Locate and identify every blood parasite.
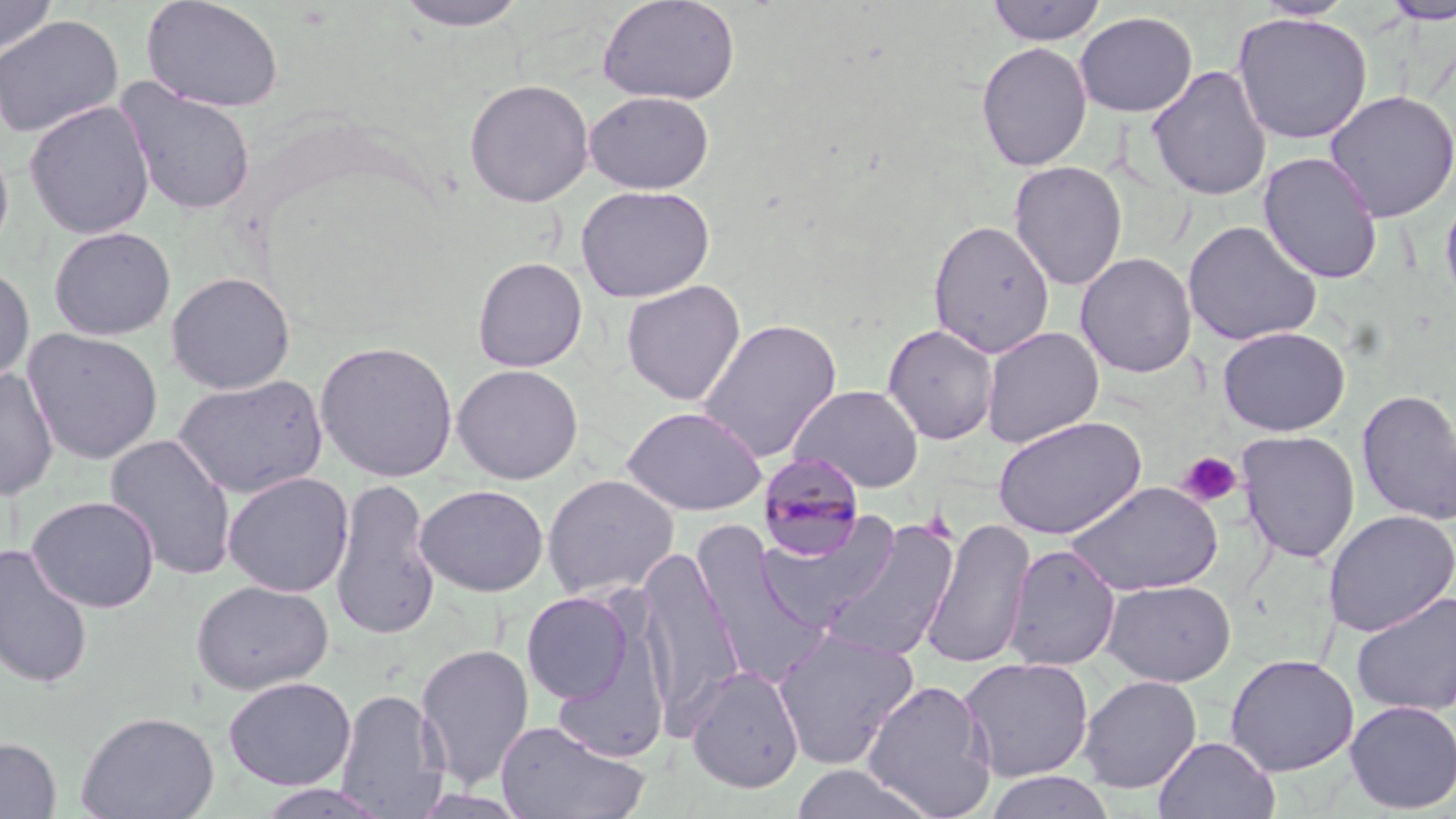
Approximate bounding boxes as named x1/y1/x2/y2 corners in pixels.
Plasmodium malariae-infected red blood cells: (x1=754, y1=453, x2=868, y2=559).
No Plasmodium falciparum, Plasmodium ovale, Plasmodium vivax, Babesia divergens, or Trypanosoma brucei observed.

Summary:
  - Uninfected red blood cell locations: (x1=0, y1=0, x2=59, y2=58), (x1=141, y1=0, x2=285, y2=113), (x1=390, y1=0, x2=533, y2=32), (x1=596, y1=0, x2=741, y2=105), (x1=985, y1=0, x2=1107, y2=46), (x1=1380, y1=0, x2=1456, y2=25), (x1=1252, y1=1, x2=1357, y2=22), (x1=1073, y1=11, x2=1198, y2=117), (x1=1231, y1=11, x2=1373, y2=145), (x1=0, y1=15, x2=124, y2=139), (x1=976, y1=41, x2=1092, y2=172), (x1=1146, y1=65, x2=1273, y2=201), (x1=463, y1=78, x2=595, y2=208), (x1=117, y1=81, x2=257, y2=217), (x1=1324, y1=89, x2=1456, y2=224), (x1=584, y1=91, x2=715, y2=194), (x1=23, y1=100, x2=156, y2=240), (x1=0, y1=131, x2=15, y2=264), (x1=1258, y1=152, x2=1383, y2=285), (x1=1008, y1=160, x2=1128, y2=291), (x1=575, y1=184, x2=716, y2=303), (x1=1440, y1=185, x2=1456, y2=314), (x1=928, y1=218, x2=1055, y2=358), (x1=1183, y1=220, x2=1323, y2=347), (x1=48, y1=226, x2=176, y2=341), (x1=1075, y1=252, x2=1197, y2=377), (x1=471, y1=256, x2=588, y2=372), (x1=0, y1=264, x2=35, y2=389), (x1=166, y1=271, x2=296, y2=395), (x1=621, y1=279, x2=746, y2=405), (x1=696, y1=317, x2=842, y2=464), (x1=882, y1=323, x2=999, y2=445), (x1=981, y1=326, x2=1104, y2=448), (x1=1218, y1=326, x2=1350, y2=436), (x1=22, y1=327, x2=163, y2=465), (x1=315, y1=339, x2=459, y2=483), (x1=452, y1=363, x2=583, y2=484), (x1=0, y1=368, x2=59, y2=501), (x1=172, y1=374, x2=328, y2=499), (x1=790, y1=384, x2=923, y2=493), (x1=1356, y1=389, x2=1456, y2=526), (x1=621, y1=405, x2=767, y2=515), (x1=992, y1=415, x2=1147, y2=540), (x1=1236, y1=430, x2=1360, y2=563), (x1=103, y1=432, x2=238, y2=580), (x1=221, y1=471, x2=354, y2=597), (x1=542, y1=473, x2=680, y2=600), (x1=330, y1=477, x2=440, y2=643), (x1=1066, y1=480, x2=1224, y2=596), (x1=415, y1=483, x2=549, y2=597), (x1=27, y1=496, x2=159, y2=612), (x1=1323, y1=510, x2=1456, y2=637), (x1=757, y1=513, x2=899, y2=630), (x1=819, y1=517, x2=960, y2=663), (x1=920, y1=517, x2=1035, y2=669), (x1=693, y1=528, x2=832, y2=688), (x1=1004, y1=542, x2=1120, y2=671), (x1=0, y1=543, x2=93, y2=689), (x1=640, y1=546, x2=745, y2=719), (x1=1100, y1=579, x2=1237, y2=687), (x1=191, y1=580, x2=334, y2=694), (x1=1349, y1=589, x2=1456, y2=717), (x1=521, y1=591, x2=635, y2=705), (x1=771, y1=627, x2=920, y2=770), (x1=415, y1=641, x2=535, y2=791), (x1=1224, y1=653, x2=1359, y2=777), (x1=958, y1=657, x2=1095, y2=783), (x1=684, y1=665, x2=804, y2=793), (x1=1078, y1=675, x2=1202, y2=794), (x1=222, y1=676, x2=356, y2=791), (x1=861, y1=678, x2=997, y2=818), (x1=334, y1=688, x2=448, y2=818), (x1=1344, y1=700, x2=1456, y2=814), (x1=75, y1=710, x2=220, y2=819), (x1=494, y1=719, x2=650, y2=819), (x1=1152, y1=735, x2=1280, y2=819), (x1=0, y1=736, x2=61, y2=819), (x1=983, y1=770, x2=1116, y2=819), (x1=251, y1=782, x2=395, y2=818)
  - Platelet locations: (x1=1177, y1=452, x2=1242, y2=507)
  - Slide-level diagnosis: Plasmodium malariae
  - Stain: May-Grünwald-Giemsa
  - Image size: 1456×819 pixels
  - Magnification: 1000x
  - Modality: optical microscopy
  - Preparation: thin blood film
  - Field of view: one of a larger specimen